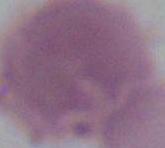

Summary:
  - Modality: photomicrograph
  - Magnification: 1000x
  - Identification: red blood cell